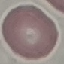

malaria status = uninfected
capture = smartphone through the microscope eyepiece
image type = automatically extracted cell patch, resized to 64 × 64 pixels
stain = Giemsa
preparation = thin smear